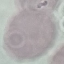 Result: no malaria parasites detected. Acquired by smartphone through the microscope eyepiece. Thin blood film. Automatically extracted cell patch, resized to 64 × 64 pixels. Giemsa-stained preparation.